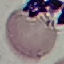
Summary:
  - Result: no malaria parasites seen
  - Capture: smartphone through the microscope eyepiece
  - Image type: cell patch, automatically extracted from a larger field of view and resized to 64 × 64 pixels
  - Stain: Giemsa
  - Preparation: thin smear